Report the malaria status of this cell.
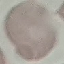

Uninfected.

Thin blood film. Giemsa-stained preparation. Acquired by smartphone through the microscope eyepiece. Automatically extracted cell patch, resized to 64 × 64 pixels.